Name the parasite shown.
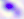

Toxoplasma gondii.

Captured at 400x magnification. Micrograph.